Describe the morphology of the red blood cells.
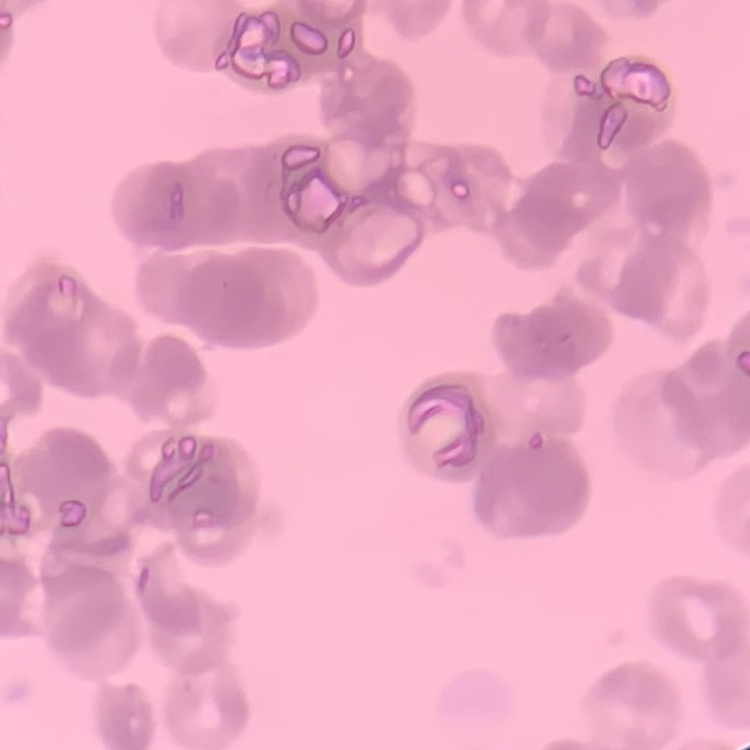

They show rouleaux formation.

Thin peripheral smear. One tile cut from a larger photomicrograph. Field's or Giemsa stain.